Name the parasite shown.
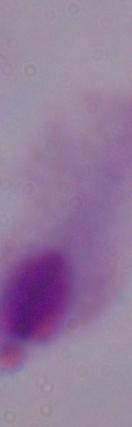

A trichomonad.

1000x magnification. Micrograph.